Name the parasite shown.
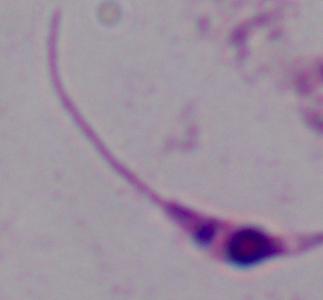
This is Leishmania.

Summary:
  - Magnification: 1000x
  - Modality: micrograph